Give the extent of all uninfected red blood cells.
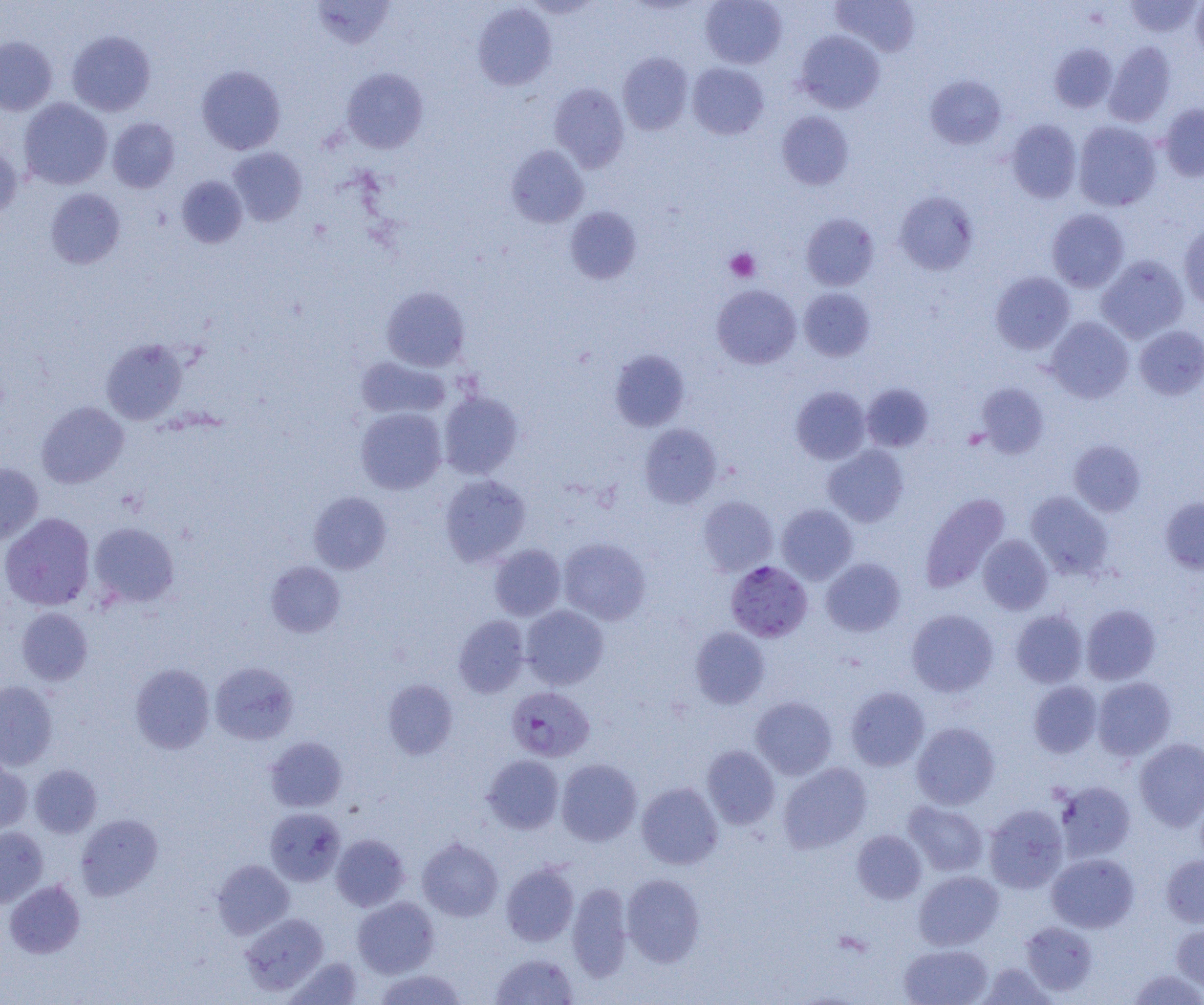
Approximate bounding boxes as (x1,y1)-(x2,y2) corner pairs in pixels.
Uninfected red blood cells: (312,0)-(395,49), (700,0)-(787,69), (832,0)-(920,56), (1192,0)-(1204,60), (1125,1)-(1201,38), (473,3)-(556,90), (67,30)-(156,116), (795,30)-(885,113), (0,36)-(57,115), (1105,41)-(1176,127), (1049,43)-(1117,113), (618,52)-(693,135), (687,63)-(768,139), (196,65)-(286,154), (341,68)-(427,153), (925,75)-(1006,150), (549,83)-(629,173), (19,98)-(112,189), (1159,103)-(1204,181), (777,111)-(854,190), (107,117)-(180,193), (1006,119)-(1082,203), (1073,121)-(1162,211), (0,142)-(22,221), (506,145)-(589,227), (227,147)-(307,226), (176,175)-(247,248), (45,188)-(125,269), (895,192)-(978,274), (565,206)-(641,284), (1046,209)-(1129,292), (801,212)-(879,290), (1179,224)-(1204,310), (1097,255)-(1188,343), (990,271)-(1075,354), (712,284)-(801,368), (381,286)-(470,371), (799,288)-(875,361), (1046,317)-(1134,402), (1134,325)-(1204,400), (101,338)-(188,425), (609,349)-(690,431), (356,356)-(450,420), (861,383)-(933,452), (976,383)-(1049,458), (791,386)-(871,464), (438,391)-(523,479), (36,401)-(128,488), (356,407)-(446,494), (639,424)-(721,509), (1069,440)-(1146,516), (823,444)-(909,527), (0,462)-(43,546), (440,474)-(530,566), (309,491)-(392,574), (1026,491)-(1113,579), (920,493)-(1010,592), (698,496)-(778,576), (1160,496)-(1204,574), (777,504)-(858,583), (0,512)-(95,610), (89,522)-(179,607), (978,534)-(1053,614), (558,538)-(651,624), (489,544)-(565,621), (821,558)-(906,636), (265,560)-(346,637), (521,605)-(608,689), (1082,605)-(1161,684), (16,607)-(93,686), (906,608)-(999,696), (1010,609)-(1088,687), (454,615)-(529,698), (690,627)-(770,709), (210,661)-(299,745), (129,664)-(215,753), (1092,677)-(1176,761), (382,679)-(458,759), (0,680)-(58,770), (1028,680)-(1102,758), (845,687)-(929,771), (750,696)-(837,779), (912,722)-(1000,809), (265,736)-(347,812), (1134,738)-(1204,831), (702,745)-(780,829), (482,755)-(564,834), (556,758)-(642,845), (0,759)-(32,834), (778,762)-(871,853), (30,764)-(102,837), (1054,781)-(1136,863), (636,782)-(723,869), (903,801)-(988,876), (984,804)-(1069,893), (265,808)-(345,886), (76,813)-(163,900), (0,826)-(48,908), (852,829)-(926,904), (331,834)-(410,911), (417,837)-(503,921), (1047,853)-(1139,933), (1161,854)-(1204,928), (212,859)-(294,939), (501,862)-(579,946), (914,870)-(1003,950), (621,873)-(705,967), (4,880)-(85,958), (567,882)-(632,980), (352,897)-(439,978), (239,913)-(329,994), (1020,920)-(1097,997), (1171,922)-(1204,993), (899,944)-(993,1005), (491,953)-(579,1004), (286,956)-(364,1004), (978,962)-(1056,1004), (374,969)-(468,1004), (1127,969)-(1204,1004).

Summary:
  - Platelet locations: (725,248)-(760,282)
  - Plasmodium falciparum-infected red blood cell locations: (726,560)-(812,642), (506,686)-(595,762)
  - Slide-level diagnosis: Plasmodium falciparum
  - Image size: 1204×1005 pixels
  - Magnification: 1000x
  - Modality: light microscopy
  - Field of view: single
  - Preparation: thin blood film